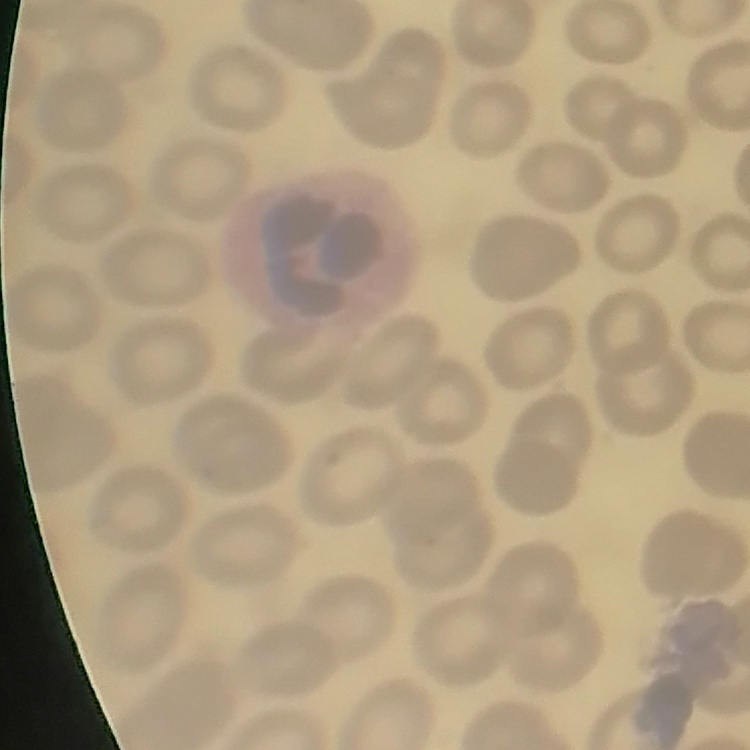

{
  "red_blood_cell_morphology": "no rouleaux formation",
  "image_type": "one tile cut from a larger photomicrograph",
  "stain": "Field's or Giemsa",
  "preparation": "thin peripheral smear"
}